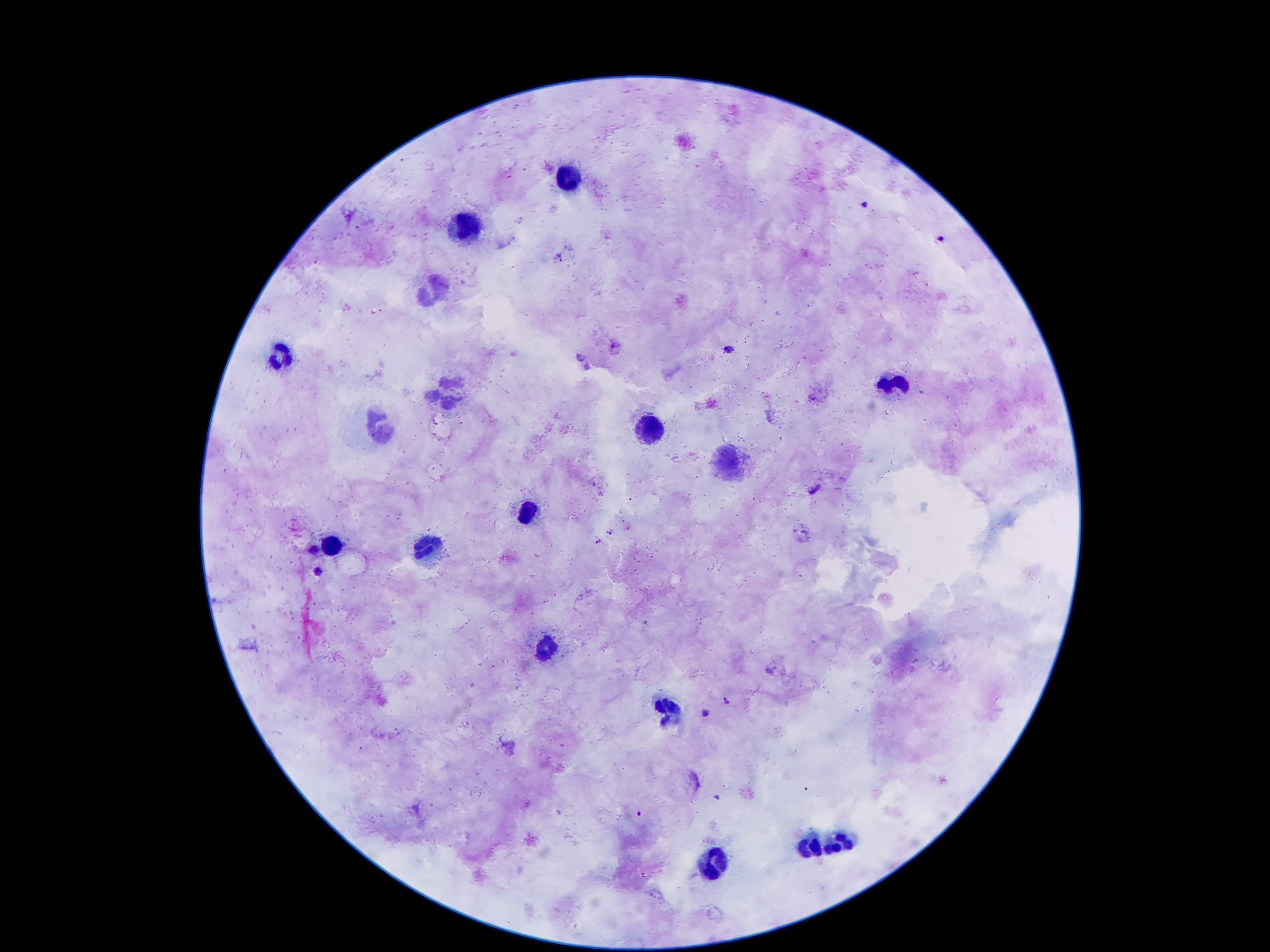

Approximate object centers, in pixels from the top-left corner.
Summary:
  - Leukocyte locations: (x=570, y=177), (x=473, y=230), (x=433, y=288), (x=278, y=356), (x=888, y=384), (x=450, y=388), (x=377, y=427), (x=647, y=432), (x=726, y=462), (x=522, y=508), (x=330, y=544), (x=427, y=544), (x=543, y=646), (x=669, y=712), (x=843, y=842), (x=807, y=844), (x=708, y=859)
  - Plasmodium parasite locations: (x=864, y=203), (x=940, y=239), (x=560, y=257), (x=729, y=349), (x=610, y=532), (x=599, y=541), (x=315, y=549), (x=318, y=573), (x=727, y=702), (x=706, y=712), (x=638, y=813)
  - Capture: smartphone through the microscope eyepiece
  - Stain: Giemsa
  - Patient malaria status: positive for Plasmodium falciparum
  - Field of view: one from this slide
  - Preparation: thick blood film
  - Magnification: 100x
  - Image size: 1270×952 pixels